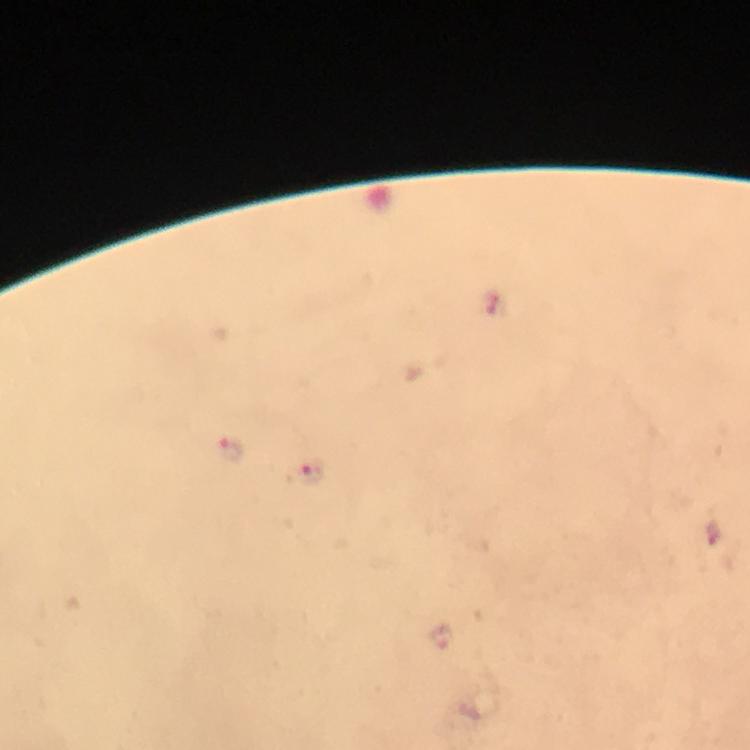

Approximate centers as (x, y) in pixels.
Summary:
  - Plasmodium parasite locations: (228, 450), (305, 473)
  - Cropped from: a single field of view
  - Stain: Giemsa
  - Preparation: thick blood film
  - Capture: smartphone camera through the microscope
  - Image size: 750×750 pixels
  - Magnification: 100x
  - Context: from a diagnostic examination for malaria
  - Immersion oil: used